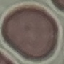
malaria status = uninfected
preparation = thin smear
image type = cell patch, automatically extracted from a larger field of view and resized to 64 × 64 pixels
capture = smartphone camera at the microscope eyepiece
stain = Giemsa